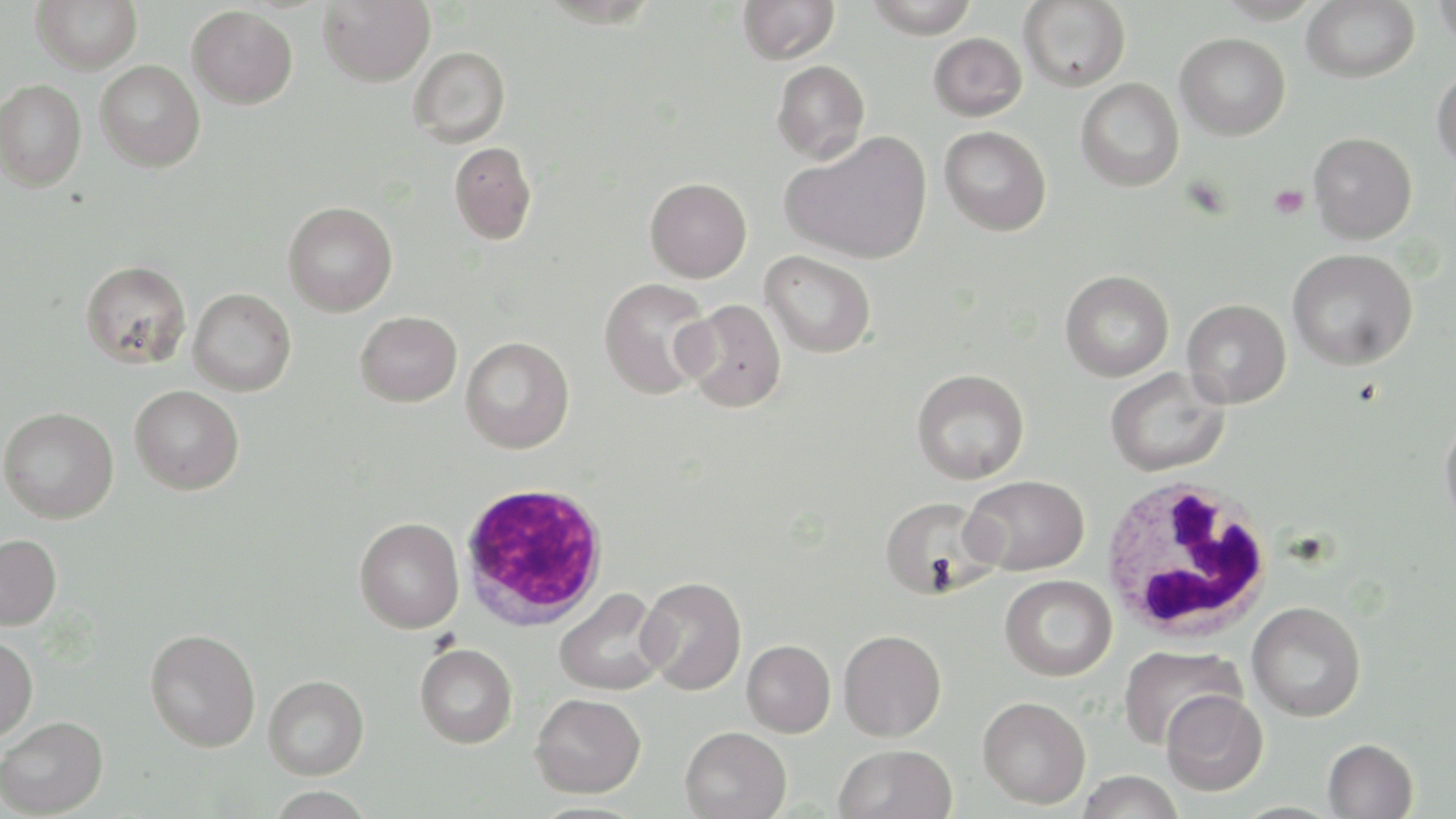
Summary:
  - Coordinate format: approximate bounding boxes as [x1, y1, x2, y2] in pixels
  - Platelet locations: [1269, 184, 1310, 219]
  - White blood cell locations: [1098, 474, 1276, 644], [459, 481, 610, 630]
  - Uninfected red blood cell locations: [31, 0, 142, 74], [318, 0, 435, 86], [737, 0, 840, 65], [863, 0, 979, 38], [1018, 0, 1130, 92], [1215, 0, 1324, 24], [1301, 0, 1419, 83], [1433, 0, 1456, 52], [187, 5, 298, 108], [928, 33, 1027, 121], [1175, 33, 1290, 141], [408, 46, 511, 147], [95, 59, 205, 171], [771, 60, 870, 164], [1432, 67, 1456, 169], [1075, 78, 1184, 192], [0, 79, 87, 192], [939, 126, 1051, 236], [782, 132, 933, 265], [1308, 132, 1417, 244], [449, 142, 537, 245], [645, 177, 752, 283], [283, 201, 398, 316], [1287, 248, 1418, 371], [760, 250, 877, 358], [80, 259, 192, 369], [1060, 270, 1174, 381], [598, 277, 714, 400], [188, 288, 296, 396], [1182, 298, 1291, 409], [678, 299, 787, 412], [355, 310, 462, 407], [460, 336, 574, 454], [911, 368, 1030, 483], [1105, 368, 1230, 476], [130, 385, 244, 495], [0, 406, 119, 524], [1439, 408, 1456, 535], [962, 474, 1089, 576], [878, 496, 999, 600], [354, 517, 464, 633], [0, 534, 62, 630], [1000, 574, 1117, 681], [638, 577, 747, 695], [554, 587, 668, 696], [1246, 601, 1366, 721], [145, 627, 261, 751], [838, 629, 946, 741], [0, 634, 38, 741], [742, 639, 836, 737], [415, 643, 517, 748], [1117, 644, 1245, 750], [263, 675, 369, 779], [1161, 690, 1268, 795], [531, 692, 646, 797], [977, 696, 1091, 809], [0, 716, 108, 817], [680, 726, 792, 819], [1323, 738, 1418, 819], [834, 744, 958, 819], [1077, 770, 1184, 819], [267, 787, 375, 818]
  - Slide-level diagnosis: Plasmodium falciparum
  - Magnification: 1000x
  - Field of view: single
  - Image size: 1456×819 pixels
  - Modality: light microscopy
  - Preparation: thin blood smear
  - Stain: May-Grünwald-Giemsa